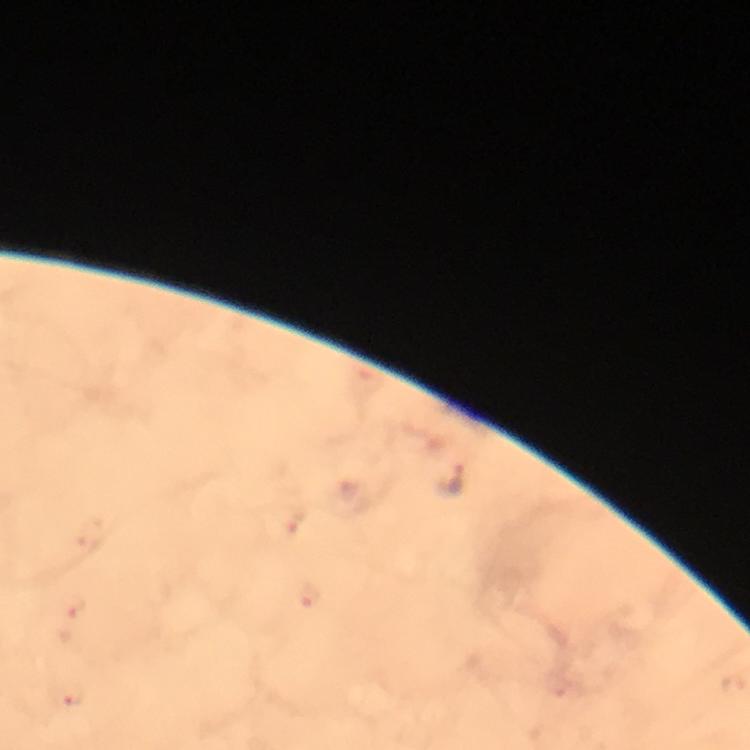
Approximate centers as [x, y] in pixels.
Summary:
  - Malaria parasite locations: [449, 480]
  - Image size: 750×750 pixels
  - Preparation: thick blood smear
  - Cropped from: a single field of view
  - Stain: Giemsa
  - Immersion oil: applied
  - Magnification: 100x
  - Context: from a diagnostic examination for malaria
  - Capture: smartphone camera through the microscope